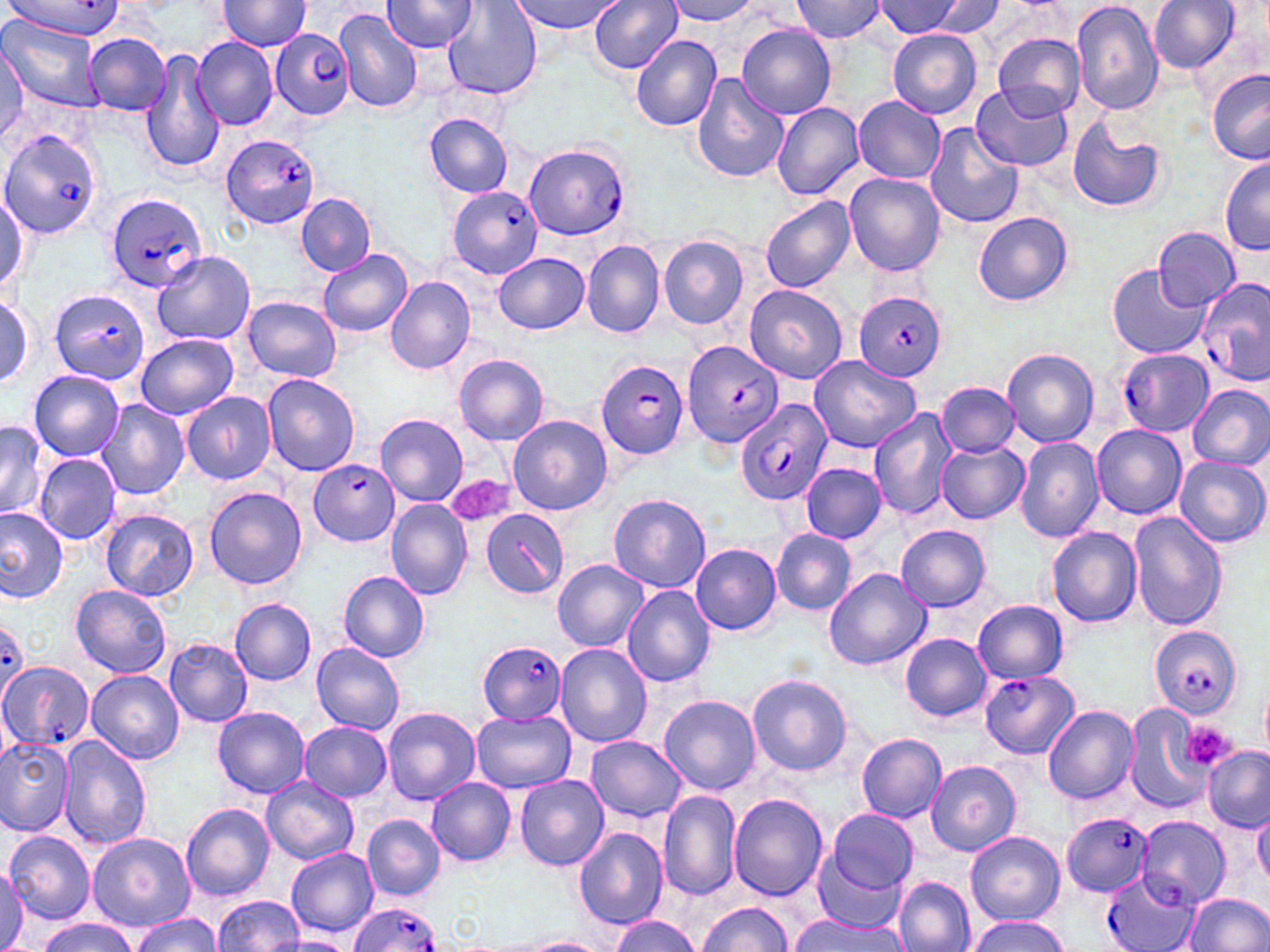
slide-level diagnosis = Plasmodium falciparum
modality = light microscopy
field of view = one of a larger specimen
uninfected red blood cell locations = approximate bounding boxes as (x1, y1, x2, y2) in pixels: (512, 0, 620, 34), (590, 0, 683, 73), (666, 0, 761, 25), (788, 0, 889, 42), (875, 0, 967, 38), (923, 0, 1005, 37), (1071, 0, 1165, 115), (1149, 0, 1240, 73), (213, 1, 313, 52), (382, 1, 479, 53), (443, 3, 541, 100), (333, 8, 423, 113), (3, 19, 105, 111), (738, 25, 836, 119), (887, 29, 982, 119), (85, 32, 171, 115), (994, 33, 1085, 118), (631, 35, 722, 132), (192, 37, 277, 130), (0, 48, 28, 142), (142, 52, 223, 175), (1206, 70, 1270, 165), (690, 73, 788, 186), (974, 83, 1075, 175), (854, 95, 947, 185), (771, 103, 864, 199), (425, 114, 513, 196), (1066, 118, 1167, 214), (925, 123, 1023, 229), (1218, 158, 1270, 256), (844, 172, 945, 279), (0, 193, 27, 289), (297, 193, 375, 275), (759, 195, 855, 293), (971, 212, 1073, 306), (1153, 226, 1240, 310), (659, 236, 749, 329), (582, 239, 665, 339), (318, 248, 412, 336), (153, 250, 255, 345), (494, 252, 590, 333), (1109, 264, 1211, 359), (385, 275, 477, 375), (744, 284, 851, 384), (1, 295, 34, 387), (243, 296, 340, 383), (135, 334, 238, 420), (1001, 347, 1099, 449), (808, 353, 922, 454), (454, 354, 550, 447), (29, 371, 124, 460), (262, 372, 361, 476), (936, 381, 1020, 457), (1188, 384, 1270, 470), (182, 391, 276, 484), (95, 399, 188, 500), (867, 407, 955, 519), (507, 414, 612, 516), (375, 415, 467, 508), (0, 420, 47, 522), (1091, 424, 1186, 519), (1016, 437, 1104, 542), (936, 441, 1027, 523), (33, 454, 120, 544), (1174, 456, 1268, 549), (800, 463, 887, 543), (204, 487, 308, 590), (608, 492, 711, 594), (384, 500, 472, 599), (0, 506, 68, 602), (102, 509, 199, 603), (1127, 512, 1227, 632), (896, 525, 991, 610), (1045, 526, 1143, 627), (770, 529, 857, 615), (690, 543, 782, 636), (553, 559, 649, 653), (823, 568, 930, 670), (339, 570, 431, 663), (621, 584, 717, 688), (71, 586, 172, 677), (231, 599, 317, 685), (974, 600, 1070, 683), (901, 633, 992, 721), (165, 638, 253, 727), (311, 642, 405, 735), (553, 642, 651, 748), (87, 670, 183, 766), (746, 674, 852, 777), (1261, 682, 1270, 756), (659, 695, 761, 795), (1124, 703, 1209, 812), (1043, 705, 1139, 803), (213, 707, 311, 798), (383, 707, 480, 805), (471, 709, 577, 793), (298, 722, 392, 802), (856, 733, 946, 823), (0, 735, 76, 835), (59, 736, 150, 852), (586, 736, 685, 821), (1202, 747, 1269, 829), (926, 760, 1021, 856), (514, 776, 609, 871), (262, 778, 358, 864), (427, 778, 516, 865), (658, 790, 741, 901), (730, 793, 828, 901), (181, 803, 275, 901), (1253, 806, 1270, 888), (826, 809, 919, 896), (362, 815, 445, 900), (1138, 817, 1228, 907), (574, 827, 668, 930), (5, 831, 95, 924), (964, 832, 1064, 926), (87, 833, 194, 931), (806, 835, 912, 932), (286, 847, 378, 938), (0, 870, 28, 948), (894, 877, 973, 952), (1184, 893, 1270, 952), (213, 895, 303, 951), (695, 903, 792, 951), (129, 913, 223, 952), (791, 913, 907, 952), (966, 915, 1070, 952), (611, 916, 702, 952), (38, 918, 136, 952), (276, 934, 354, 952), (525, 937, 612, 952)
preparation = thin blood film
Plasmodium falciparum-infected red blood cell locations (subset) = approximate bounding boxes as (x1, y1, x2, y2) in pixels: (7, 0, 127, 40), (270, 28, 354, 118), (0, 129, 102, 242), (220, 134, 320, 228), (522, 141, 630, 241), (450, 184, 544, 279), (103, 191, 210, 293), (1196, 276, 1269, 388), (49, 288, 151, 386), (853, 291, 945, 381), (681, 340, 783, 448), (1116, 348, 1214, 435), (595, 357, 690, 459), (734, 397, 832, 506), (311, 461, 400, 546), (0, 621, 30, 698), (1149, 626, 1243, 719), (477, 641, 567, 725), (0, 662, 93, 753), (980, 670, 1078, 758), (1060, 812, 1152, 896), (1102, 873, 1197, 952), (347, 904, 443, 952)
stain = May-Grünwald-Giemsa
image size = 1270×952 pixels
magnification = 1000x
platelet locations (subset) = approximate bounding boxes as (x1, y1, x2, y2) in pixels: (1183, 722, 1238, 770)